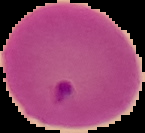
Summary:
  - Preparation: thin blood film
  - Malaria status: parasitized
  - Image size: 145×133 pixels
  - Image type: segmented cell region on a black background